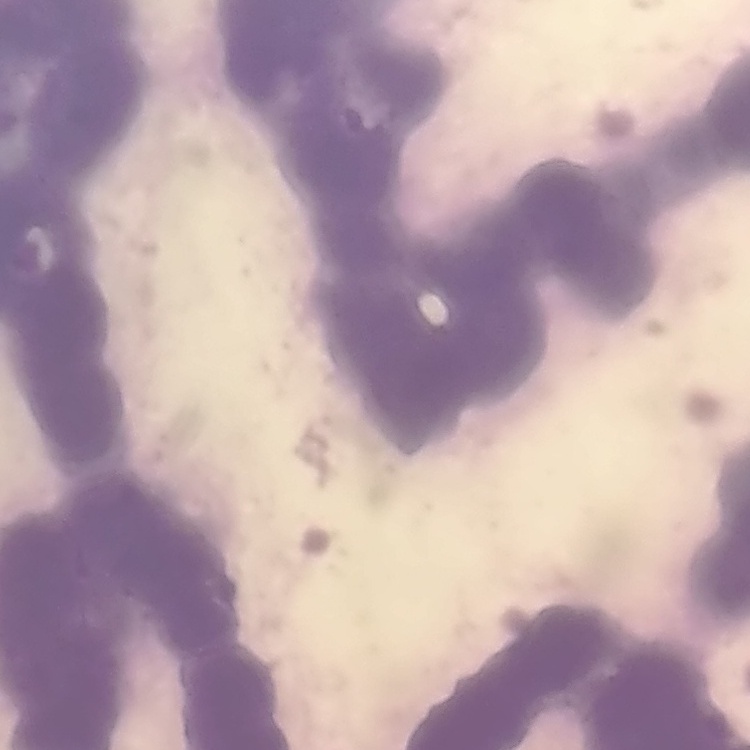
red_blood_cell_morphology: rouleaux formation
preparation: thin blood smear
image_type: one tile cut from a larger photomicrograph
stain: Field's or Giemsa